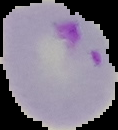
preparation = thin blood film
image type = segmented cell region with the area outside set to black
malaria status = parasitized
image size = 118×130 pixels